Describe the morphology of the red blood cells.
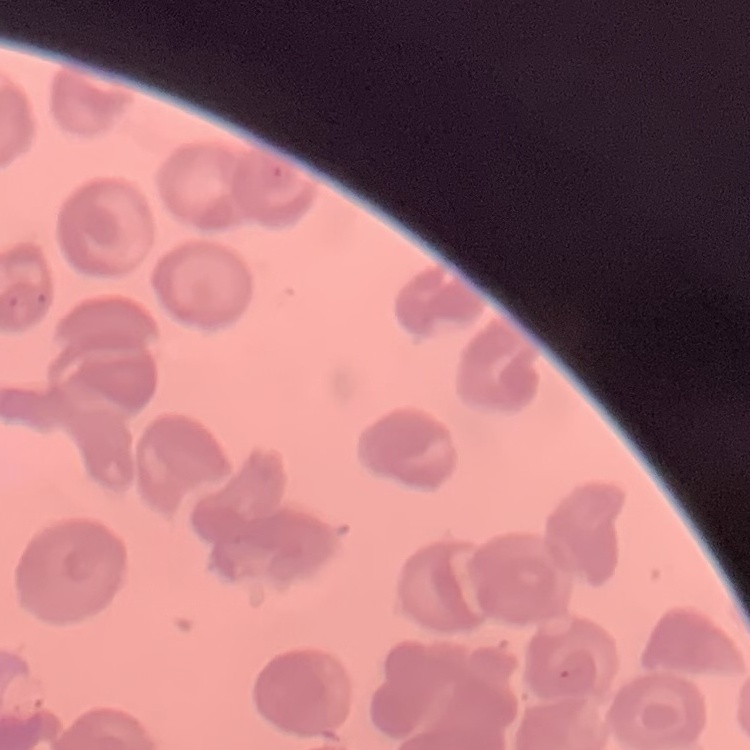
They show no rouleaux formation.

Thin peripheral smear. Square crop of a larger photomicrograph. Field's or Giemsa stain.